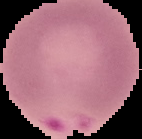 From a thin blood smear. Result: malaria parasites identified. Cell region segmented out of the field of view; the surrounding area is masked to black. Image is 142×139 pixels.